State which parasite is depicted.
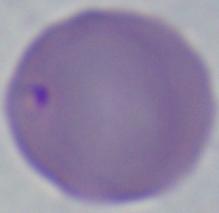
Babesia.

1000x magnification. Micrograph.